State which parasite is depicted.
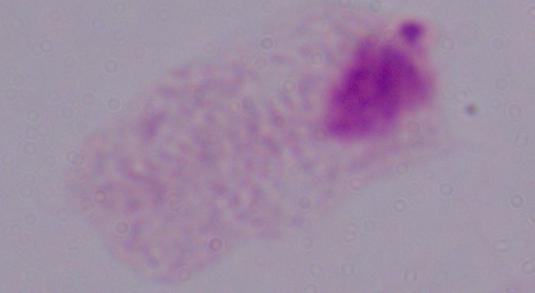

A trichomonad.

Summary:
  - Modality: photomicrograph
  - Magnification: 1000x